Identify the parasite.
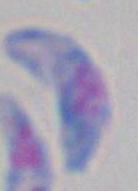
This is Toxoplasma gondii.

Micrograph. Captured at 1000x magnification.